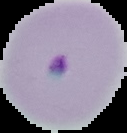
Segmented cell region on a black background. Malaria status: parasitized. Image is 127×133 pixels. From a thin blood film.